State which parasite is depicted.
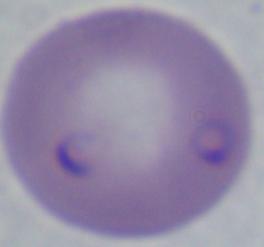

Babesia.

modality = micrograph
magnification = 1000x